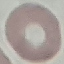

Summary:
  - Malaria status: uninfected
  - Image type: automatically extracted cell patch, resized to 64 × 64 pixels
  - Stain: Giemsa
  - Preparation: thin blood smear
  - Capture: smartphone camera at the microscope eyepiece